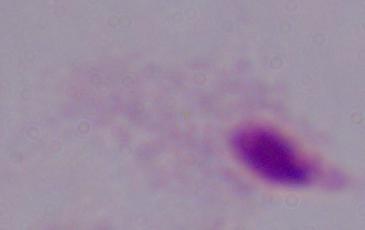

A trichomonad is seen. 1000x magnification. Micrograph.